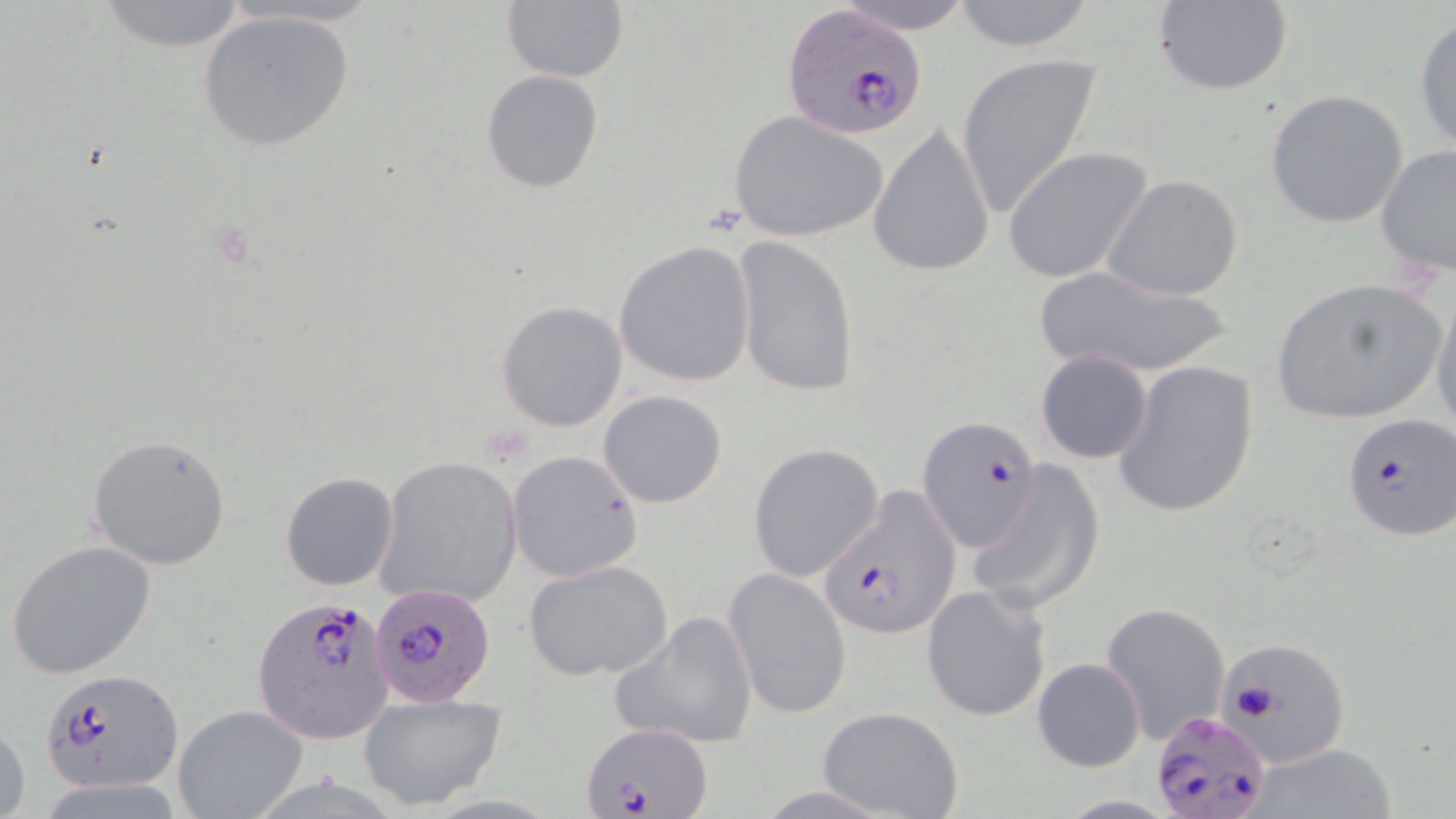

Summary:
  - Coordinate format: approximate bounding boxes as named x1/y1/x2/y2 corners in pixels
  - Plasmodium falciparum-infected red blood cell locations: (x1=780, y1=4, x2=926, y2=140), (x1=1340, y1=414, x2=1456, y2=540), (x1=919, y1=415, x2=1043, y2=552), (x1=819, y1=486, x2=959, y2=642), (x1=370, y1=581, x2=497, y2=708), (x1=250, y1=596, x2=394, y2=745), (x1=1212, y1=638, x2=1352, y2=771), (x1=40, y1=667, x2=183, y2=793), (x1=1145, y1=713, x2=1270, y2=819), (x1=581, y1=723, x2=708, y2=817)
  - Uninfected red blood cell locations: (x1=90, y1=0, x2=254, y2=52), (x1=826, y1=0, x2=979, y2=34), (x1=946, y1=0, x2=1102, y2=52), (x1=1152, y1=0, x2=1295, y2=98), (x1=500, y1=2, x2=629, y2=83), (x1=197, y1=9, x2=357, y2=152), (x1=1413, y1=13, x2=1456, y2=158), (x1=955, y1=53, x2=1105, y2=222), (x1=480, y1=70, x2=604, y2=194), (x1=1264, y1=89, x2=1409, y2=230), (x1=729, y1=110, x2=889, y2=244), (x1=869, y1=123, x2=996, y2=277), (x1=1375, y1=142, x2=1456, y2=278), (x1=1005, y1=147, x2=1154, y2=285), (x1=1101, y1=173, x2=1246, y2=300), (x1=732, y1=235, x2=861, y2=397), (x1=613, y1=240, x2=757, y2=388), (x1=1034, y1=264, x2=1239, y2=379), (x1=1267, y1=275, x2=1447, y2=427), (x1=1428, y1=284, x2=1456, y2=444), (x1=496, y1=300, x2=628, y2=432), (x1=1036, y1=350, x2=1154, y2=464), (x1=1114, y1=358, x2=1259, y2=518), (x1=597, y1=389, x2=729, y2=509), (x1=86, y1=434, x2=232, y2=570), (x1=747, y1=442, x2=885, y2=583), (x1=506, y1=449, x2=644, y2=581), (x1=375, y1=456, x2=523, y2=607), (x1=969, y1=460, x2=1104, y2=612), (x1=280, y1=471, x2=399, y2=590), (x1=5, y1=540, x2=158, y2=679), (x1=524, y1=560, x2=673, y2=682), (x1=724, y1=567, x2=851, y2=720), (x1=922, y1=583, x2=1052, y2=723), (x1=1099, y1=601, x2=1230, y2=742), (x1=611, y1=609, x2=759, y2=750), (x1=1032, y1=656, x2=1145, y2=771), (x1=358, y1=691, x2=507, y2=811), (x1=172, y1=704, x2=310, y2=817), (x1=817, y1=706, x2=965, y2=819), (x1=0, y1=720, x2=30, y2=819), (x1=1249, y1=743, x2=1400, y2=819)
  - Slide-level diagnosis: Plasmodium falciparum
  - Modality: optical microscopy
  - Magnification: 1000x
  - Image size: 1456×819 pixels
  - Preparation: thin blood smear
  - Stain: May-Grünwald-Giemsa
  - Field of view: single